Locate every uninfected red blood cell.
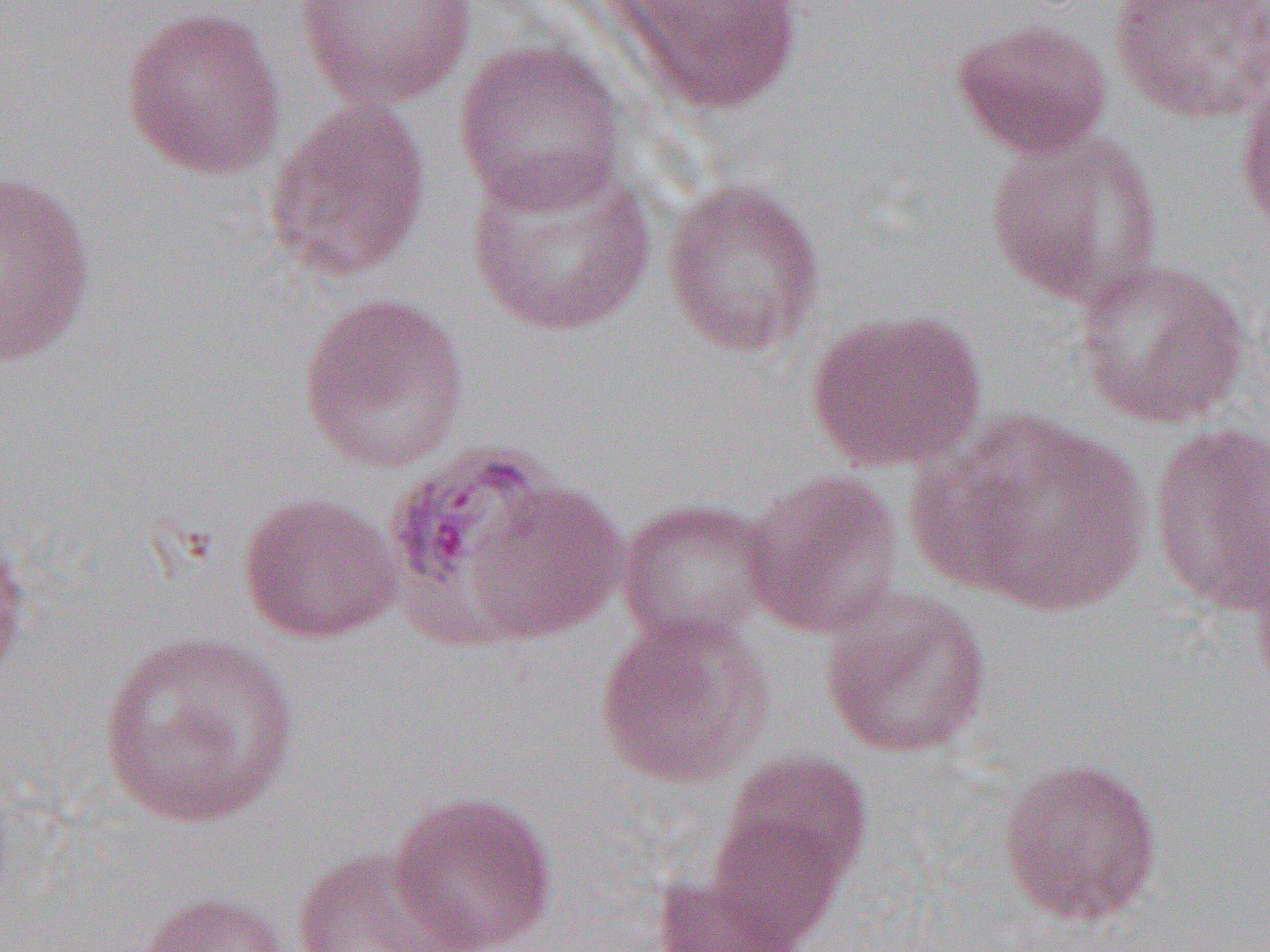
Approximate bounding boxes as named x1/y1/x2/y2 corners in pixels.
Uninfected red blood cells: (x1=603, y1=0, x2=806, y2=115), (x1=1108, y1=0, x2=1270, y2=125), (x1=293, y1=1, x2=479, y2=110), (x1=120, y1=5, x2=287, y2=179), (x1=951, y1=16, x2=1112, y2=159), (x1=453, y1=39, x2=628, y2=215), (x1=1234, y1=77, x2=1270, y2=240), (x1=264, y1=101, x2=432, y2=282), (x1=983, y1=126, x2=1166, y2=309), (x1=464, y1=156, x2=659, y2=338), (x1=0, y1=170, x2=98, y2=368), (x1=661, y1=177, x2=826, y2=357), (x1=1073, y1=259, x2=1251, y2=429), (x1=298, y1=292, x2=470, y2=474), (x1=805, y1=307, x2=986, y2=474), (x1=929, y1=409, x2=1152, y2=616), (x1=1148, y1=422, x2=1270, y2=618), (x1=741, y1=469, x2=905, y2=639), (x1=460, y1=477, x2=629, y2=644), (x1=238, y1=491, x2=404, y2=643), (x1=616, y1=497, x2=777, y2=652), (x1=0, y1=527, x2=31, y2=690), (x1=1249, y1=539, x2=1270, y2=702), (x1=819, y1=587, x2=993, y2=759), (x1=595, y1=613, x2=774, y2=789), (x1=95, y1=629, x2=301, y2=829), (x1=717, y1=750, x2=874, y2=896), (x1=997, y1=756, x2=1164, y2=928), (x1=387, y1=789, x2=559, y2=952), (x1=704, y1=807, x2=850, y2=947), (x1=289, y1=845, x2=469, y2=952), (x1=651, y1=874, x2=803, y2=952), (x1=136, y1=890, x2=293, y2=952).

Slide-level diagnosis: Plasmodium vivax. Image is 1270×952 pixels. Single field of view. Optical microscopy. Thin blood smear. 1000x magnification.